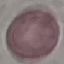 Result: no malaria parasites seen. Thin smear of blood. Giemsa-stained preparation. Photographed with a smartphone camera at the microscope eyepiece. Cell patch, automatically extracted from a larger field of view and resized to 64 × 64 pixels.